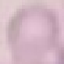

result = no malaria parasites detected
capture = smartphone through the microscope eyepiece
image type = cell patch, automatically extracted from a larger field of view and resized to 64 × 64 pixels
preparation = thin blood smear
stain = Giemsa